Outline each uninfected red blood cell.
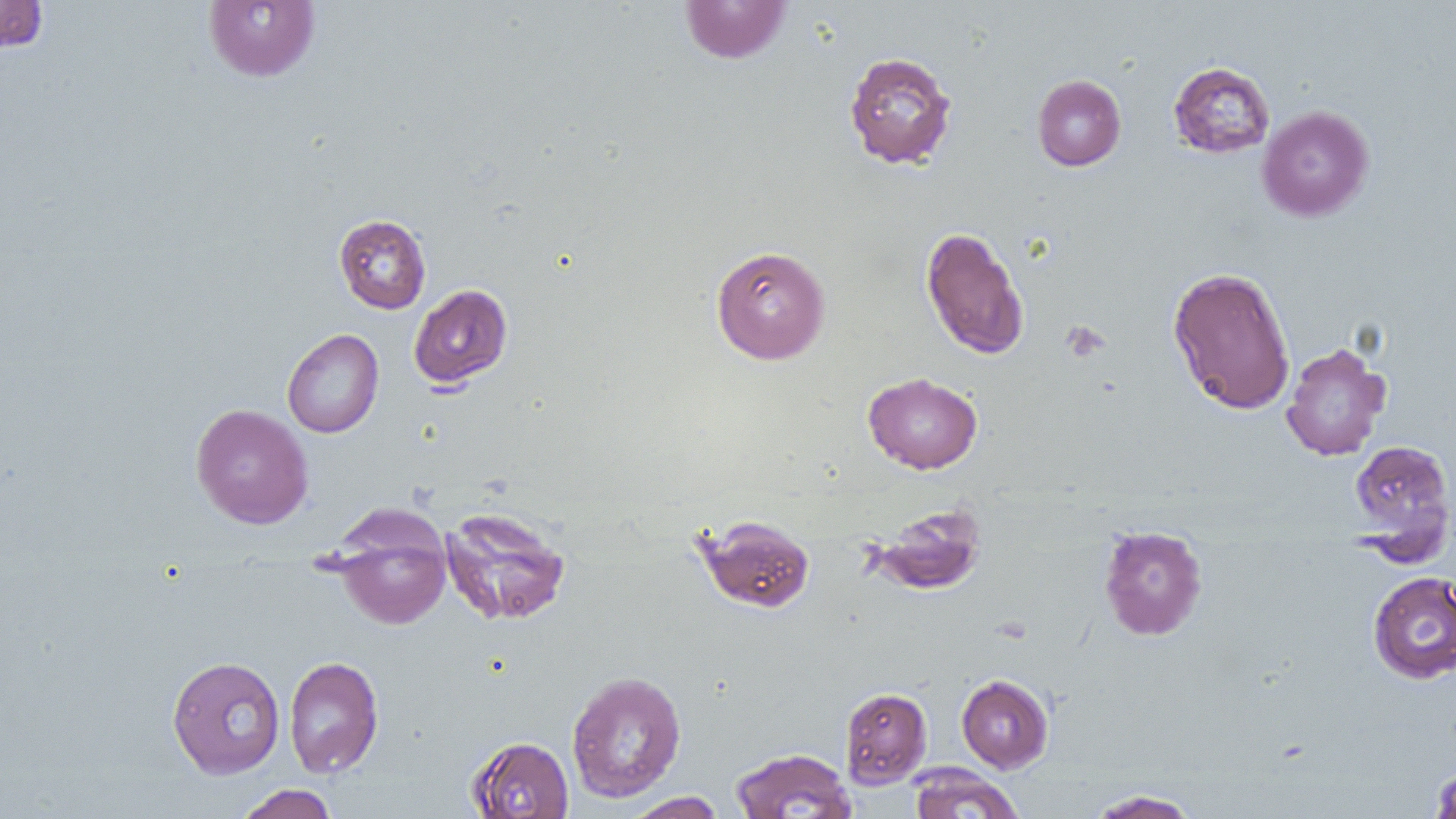
Approximate bounding boxes as (x1,y1)-(x2,y2) corner pairs in pixels.
Uninfected red blood cells: (0,0)-(48,54), (204,1)-(320,82), (680,1)-(792,64), (844,51)-(958,170), (1168,61)-(1276,159), (1032,74)-(1126,171), (1257,105)-(1374,222), (334,214)-(431,314), (920,226)-(1030,360), (711,245)-(830,364), (1167,266)-(1296,415), (409,284)-(512,389), (282,329)-(384,438), (1280,341)-(1392,461), (863,371)-(983,474), (190,403)-(314,529), (1349,439)-(1455,552), (868,503)-(987,595), (440,506)-(571,626), (332,514)-(451,630), (695,514)-(815,613), (1098,524)-(1208,641), (1367,570)-(1456,683), (283,655)-(384,778), (167,656)-(285,778), (566,670)-(686,803), (956,673)-(1054,773), (839,687)-(932,788), (466,735)-(574,818), (730,747)-(856,819), (907,763)-(1025,819), (1430,766)-(1456,818), (234,784)-(340,819), (1086,789)-(1202,818), (624,792)-(727,818).

Slide-level diagnosis: negative for blood parasites. Thin blood film. Light microscopy. Captured at 1000x magnification. One field of a larger specimen. Image is 1456×819 pixels.